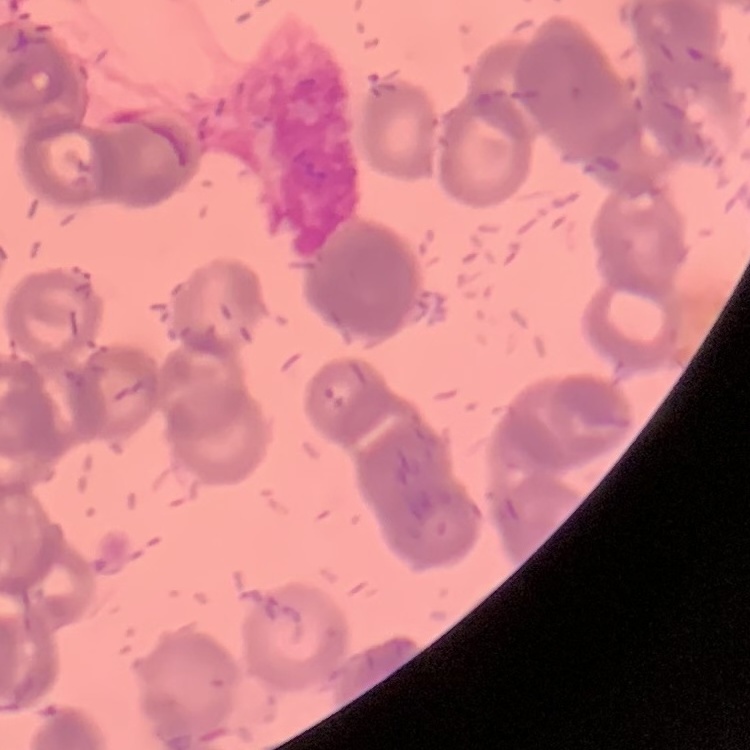
red blood cell morphology = rouleaux formation
stain = Field's or Giemsa
preparation = thin blood smear
image type = square crop of a larger photomicrograph